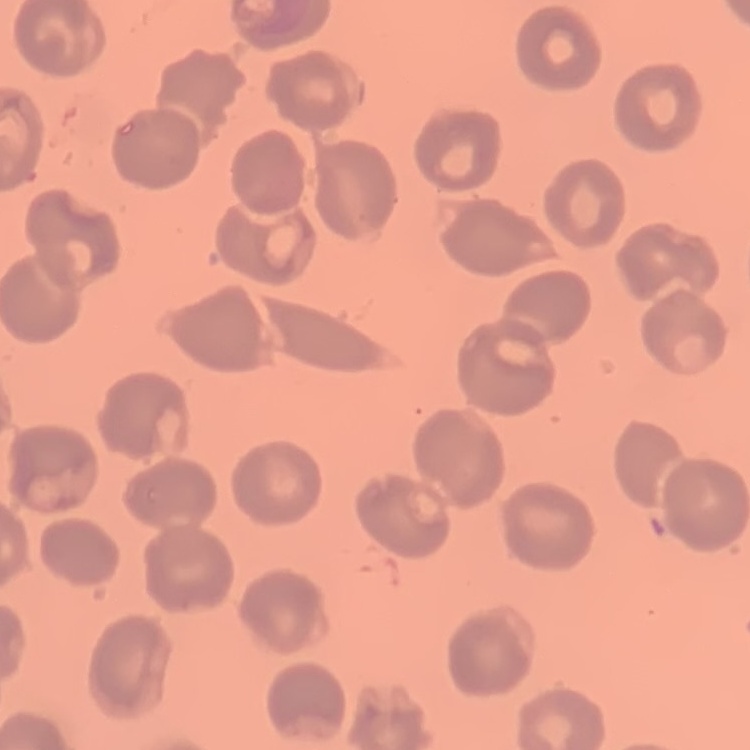

The red blood cells exhibit no rouleaux formation. Field's or Giemsa stain. Square crop of a larger photomicrograph. Thin blood film.